Describe the morphology of the red blood cells.
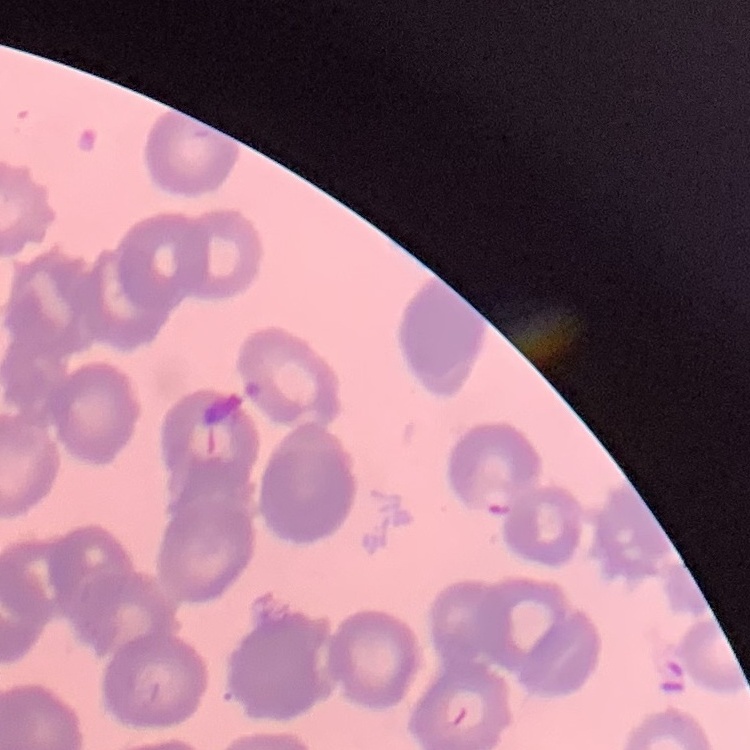

They show rouleaux formation.

Summary:
  - Preparation: thin blood film
  - Stain: Field's or Giemsa
  - Image type: square crop of a larger photomicrograph